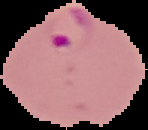

From a thin blood film. The area outside the segmented cell region is set to black. Image is 148×130 pixels. Malaria status: parasitized.